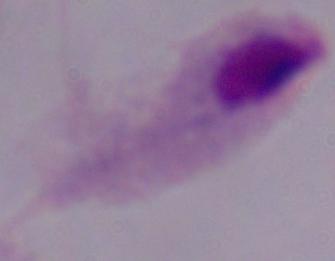

{
  "identification": "trichomonad",
  "magnification": "1000x",
  "modality": "photomicrograph"
}